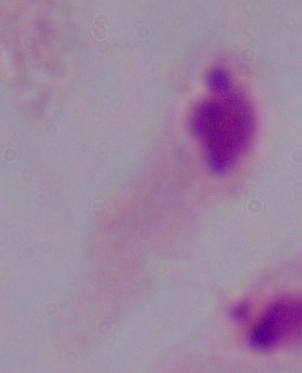

Summary:
  - Identification: trichomonad
  - Magnification: 1000x
  - Modality: photomicrograph